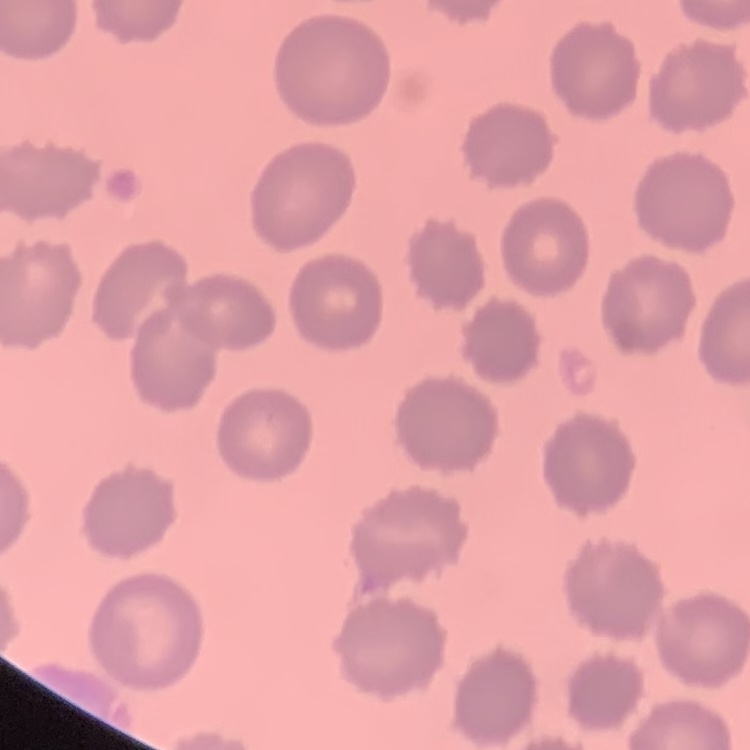

erythrocyte_morphology: no rouleaux formation
stain: Field's or Giemsa
preparation: thin blood smear
image_type: square crop of a larger photomicrograph